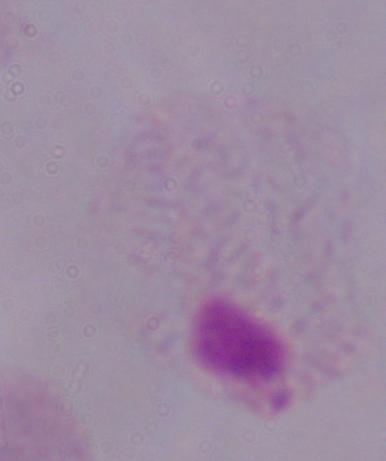 1000x magnification. A trichomonad is seen. Photomicrograph.